Locate every Plasmodium parasite.
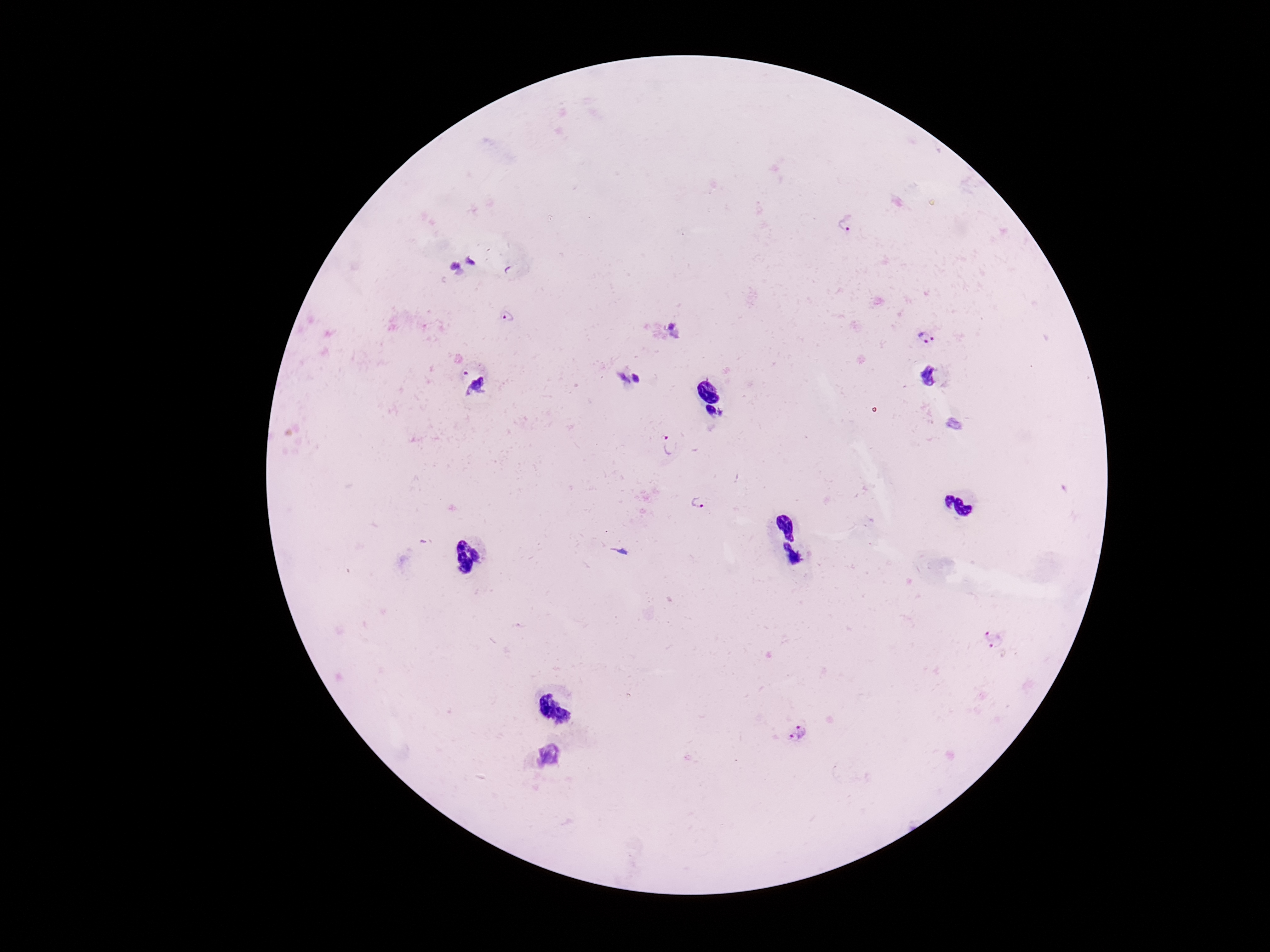
Approximate centers as {x, y} in pixels.
Plasmodium parasites: {847, 223}, {470, 259}, {455, 265}, {508, 316}, {670, 325}, {675, 337}, {927, 337}, {929, 375}, {637, 378}, {623, 379}, {478, 388}, {723, 412}, {954, 424}, {670, 445}, {699, 502}, {994, 639}, {797, 732}.

{
  "stain": "Giemsa",
  "field_of_view": "one from this slide",
  "preparation": "thick peripheral-blood smear",
  "capture": "smartphone camera through the microscope eyepiece",
  "magnification": "100x",
  "patient_malaria_status": "infected",
  "image_size": "1270×952 pixels"
}